Assess this cell for malaria.
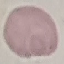
Uninfected.

Summary:
  - Capture: smartphone through the microscope eyepiece
  - Preparation: thin blood smear
  - Stain: Giemsa
  - Image type: cell patch, automatically extracted from a larger field of view and resized to 64 × 64 pixels